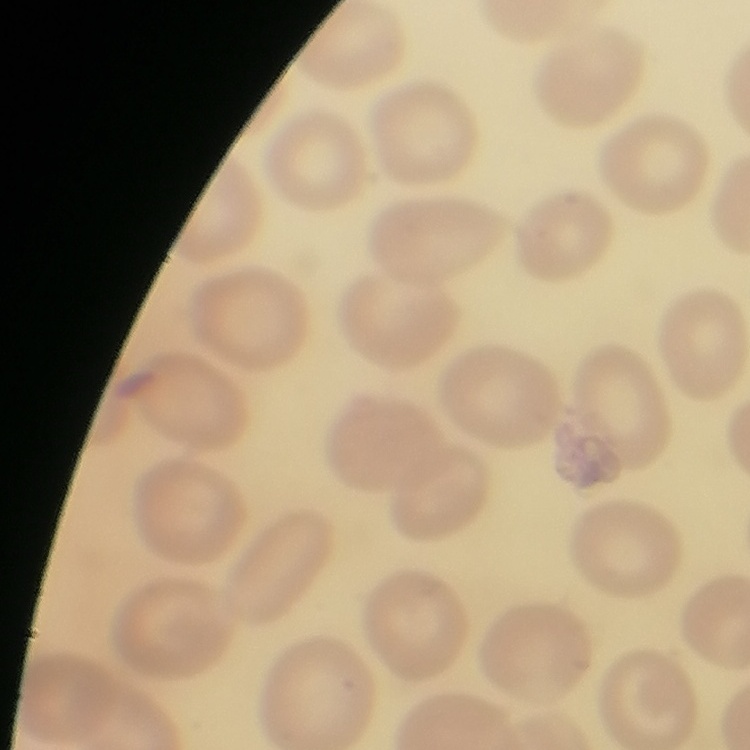

Summary:
  - Erythrocyte morphology: no rouleaux formation
  - Stain: Field's or Giemsa
  - Preparation: thin blood smear
  - Image type: one tile cut from a larger photomicrograph